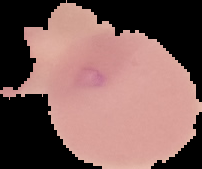

Summary:
  - Image type: cell region segmented out of the field of view; surrounding area masked to black
  - Preparation: thin blood film
  - Image size: 202×169 pixels
  - Malaria status: uninfected